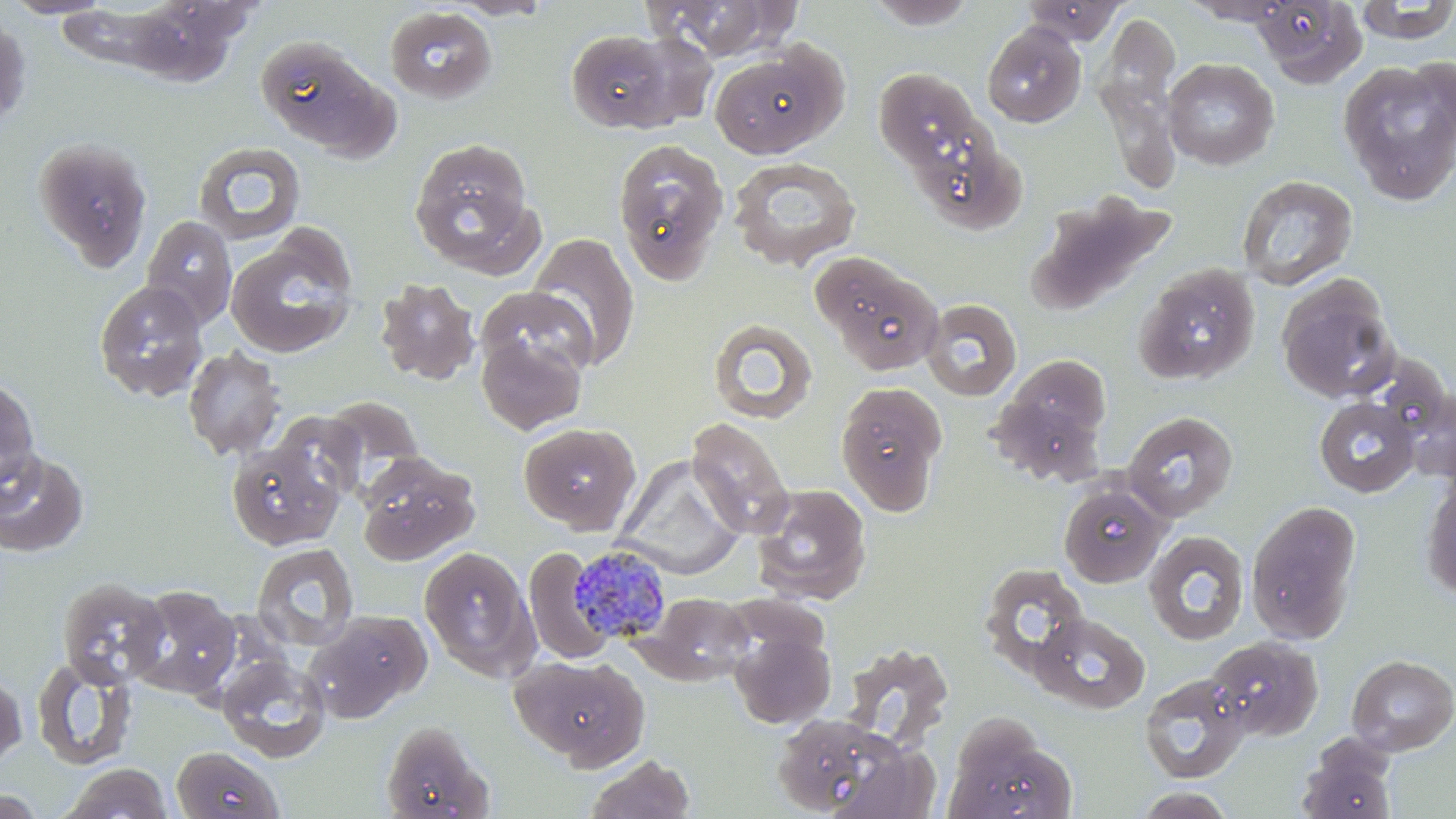
slide-level diagnosis = Plasmodium malariae
image size = 1456×819 pixels
preparation = thin blood film
field of view = one of a larger specimen
stain = May-Grünwald-Giemsa
Plasmodium malariae-infected red blood cell locations = approximate bounding boxes as (x1,y1)-(x2,y2) corner pairs in pixels: (567,544)-(674,644)
modality = light microscopy
uninfected red blood cell locations = approximate bounding boxes as (x1,y1)-(x2,y2) corner pairs in pixels: (1,0)-(116,19), (117,0)-(246,87), (448,0)-(555,20), (647,0)-(798,61), (862,0)-(980,29), (1251,0)-(1368,86), (1355,0)-(1456,45), (1021,1)-(1127,45), (384,6)-(498,105), (1096,12)-(1181,137), (0,15)-(31,128), (982,22)-(1087,128), (563,28)-(686,134), (257,37)-(394,155), (708,43)-(845,159), (1097,54)-(1184,199), (1163,58)-(1279,170), (1337,58)-(1456,204), (873,68)-(987,173), (34,138)-(152,271), (408,138)-(537,272), (613,138)-(729,285), (193,141)-(306,245), (728,157)-(861,271), (1236,174)-(1358,290), (1027,191)-(1174,316), (140,214)-(238,329), (226,231)-(358,359), (526,231)-(641,370), (812,252)-(943,376), (1133,263)-(1260,385), (1276,276)-(1399,402), (374,277)-(480,386), (93,280)-(209,402), (476,286)-(597,383), (921,298)-(1022,402), (707,318)-(818,424), (476,331)-(587,436), (183,346)-(285,460), (0,377)-(40,499), (988,378)-(1112,483), (835,381)-(948,515), (1400,386)-(1456,483), (320,395)-(425,494), (1314,397)-(1419,496), (271,410)-(366,506), (1123,410)-(1239,522), (687,417)-(794,539), (519,422)-(640,533), (226,440)-(342,551), (0,449)-(89,558), (357,452)-(479,564), (614,456)-(744,580), (1421,474)-(1456,603), (1058,482)-(1168,587), (751,484)-(872,605), (1245,500)-(1362,644), (1143,530)-(1250,645), (251,542)-(359,651), (419,545)-(537,679), (523,547)-(613,666), (980,563)-(1089,677), (56,576)-(170,688), (127,585)-(241,699), (638,591)-(754,684), (306,610)-(430,722), (1031,612)-(1151,713), (730,630)-(836,729), (1206,635)-(1323,742), (839,642)-(955,752), (510,653)-(649,768), (1346,653)-(1456,756), (218,654)-(331,763), (31,656)-(137,771), (0,670)-(27,770), (1139,672)-(1250,785), (770,713)-(917,818), (380,721)-(493,819), (943,721)-(1077,819), (170,744)-(286,819), (1297,745)-(1396,819), (584,754)-(696,819), (60,763)-(174,819), (1131,786)-(1239,818), (0,788)-(44,818)
magnification = 1000x